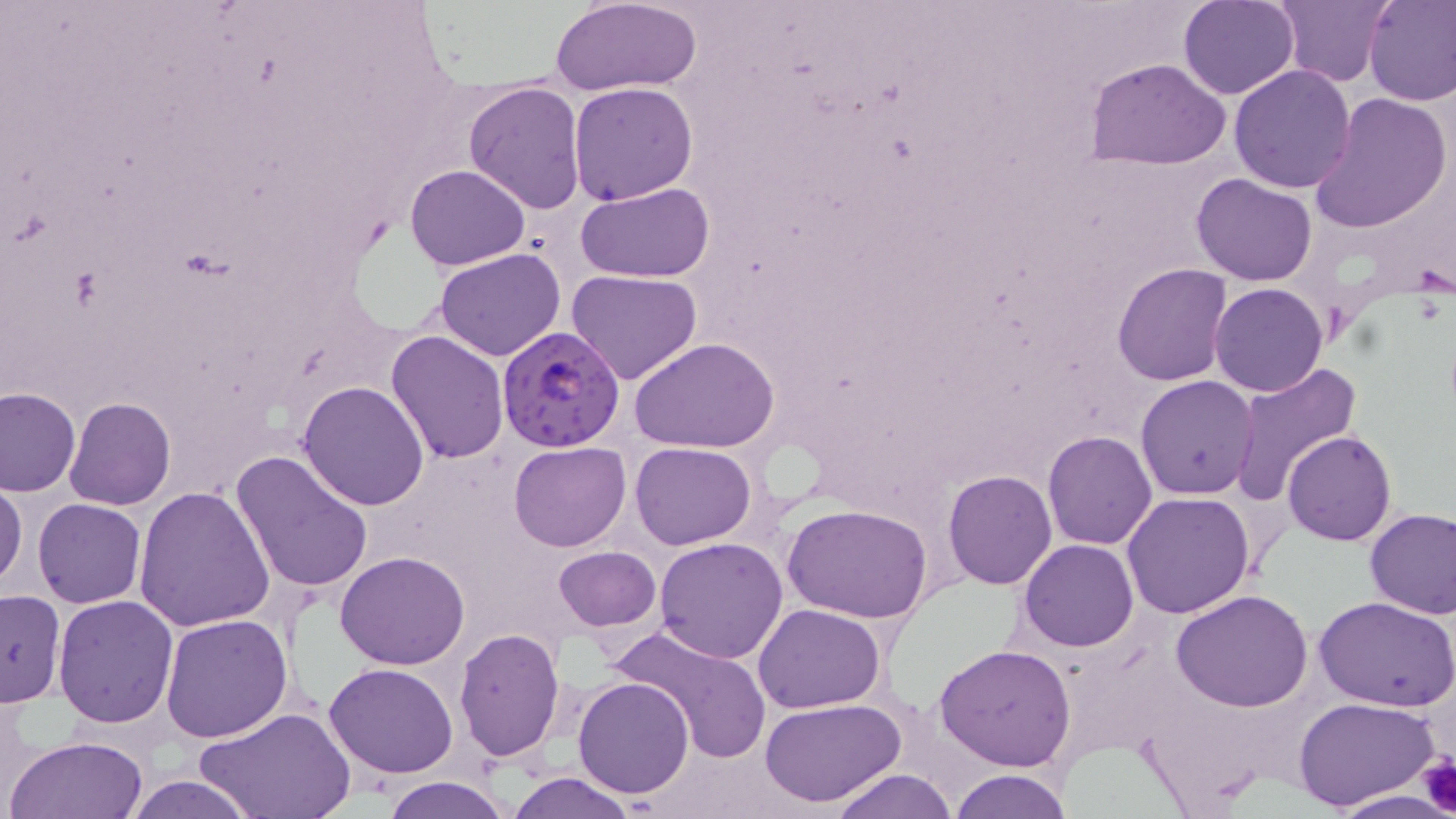
Summary:
  - Coordinate format: approximate bounding boxes as [x1, y1, x2, y2] in pixels
  - Uninfected red blood cell locations: [1178, 0, 1300, 100], [1274, 0, 1392, 87], [1364, 0, 1456, 106], [549, 1, 702, 98], [1084, 57, 1233, 169], [1229, 64, 1357, 193], [462, 82, 587, 215], [568, 82, 697, 207], [1309, 93, 1452, 233], [403, 164, 530, 271], [1191, 172, 1317, 284], [575, 184, 716, 283], [434, 249, 566, 362], [1113, 264, 1233, 386], [565, 270, 702, 386], [1209, 283, 1328, 398], [385, 330, 511, 465], [631, 337, 780, 455], [1228, 361, 1361, 502], [1135, 376, 1260, 500], [298, 380, 431, 509], [1, 386, 81, 496], [65, 397, 176, 510], [1042, 430, 1156, 550], [1283, 430, 1397, 547], [508, 440, 632, 551], [629, 441, 758, 550], [229, 451, 373, 595], [942, 470, 1057, 590], [0, 479, 25, 594], [132, 486, 277, 632], [1121, 491, 1256, 618], [31, 499, 147, 608], [785, 504, 932, 624], [1364, 506, 1456, 619], [654, 537, 789, 663], [1020, 539, 1137, 653], [552, 546, 662, 631], [334, 550, 470, 669], [1172, 589, 1315, 712], [0, 590, 65, 708], [53, 594, 179, 727], [1312, 595, 1455, 712], [752, 602, 886, 714], [160, 612, 293, 742], [610, 621, 773, 763], [454, 626, 566, 762], [934, 642, 1079, 771], [324, 662, 458, 779], [572, 677, 695, 799], [759, 696, 907, 808], [1293, 696, 1441, 812], [199, 708, 353, 819], [6, 734, 150, 819], [827, 768, 956, 818], [948, 769, 1073, 819], [505, 773, 637, 819], [124, 775, 258, 819], [383, 776, 512, 819], [1327, 790, 1455, 819]
  - Platelet locations: [1418, 755, 1456, 817]
  - Plasmodium falciparum-infected red blood cell locations: [497, 326, 624, 452]
  - Slide-level diagnosis: Plasmodium falciparum
  - Preparation: thin blood film
  - Stain: May-Grünwald-Giemsa
  - Magnification: 1000x
  - Image size: 1456×819 pixels
  - Modality: optical microscopy
  - Field of view: single